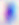

Summary:
  - Identification: Toxoplasma gondii
  - Modality: micrograph
  - Magnification: 400x